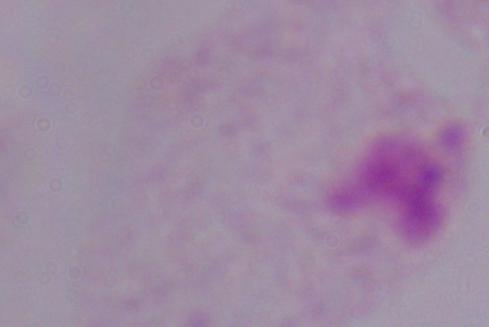
A trichomonad is seen. Photomicrograph. Captured at 1000x magnification.